Identify the cell.
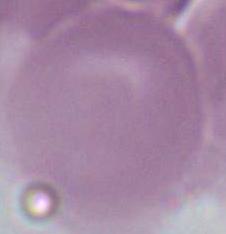
This is an erythrocyte.

1000x magnification. Photomicrograph.